Name the parasite shown.
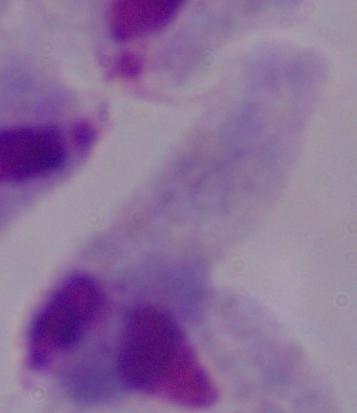

This is a trichomonad.

Summary:
  - Modality: photomicrograph
  - Magnification: 1000x